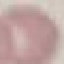 Result: no malaria parasites seen. Acquired by smartphone through the microscope eyepiece. Cell patch, automatically extracted from a larger field of view and resized to 64 × 64 pixels. Giemsa stain. Thin smear of blood.